Identify the preparation type.
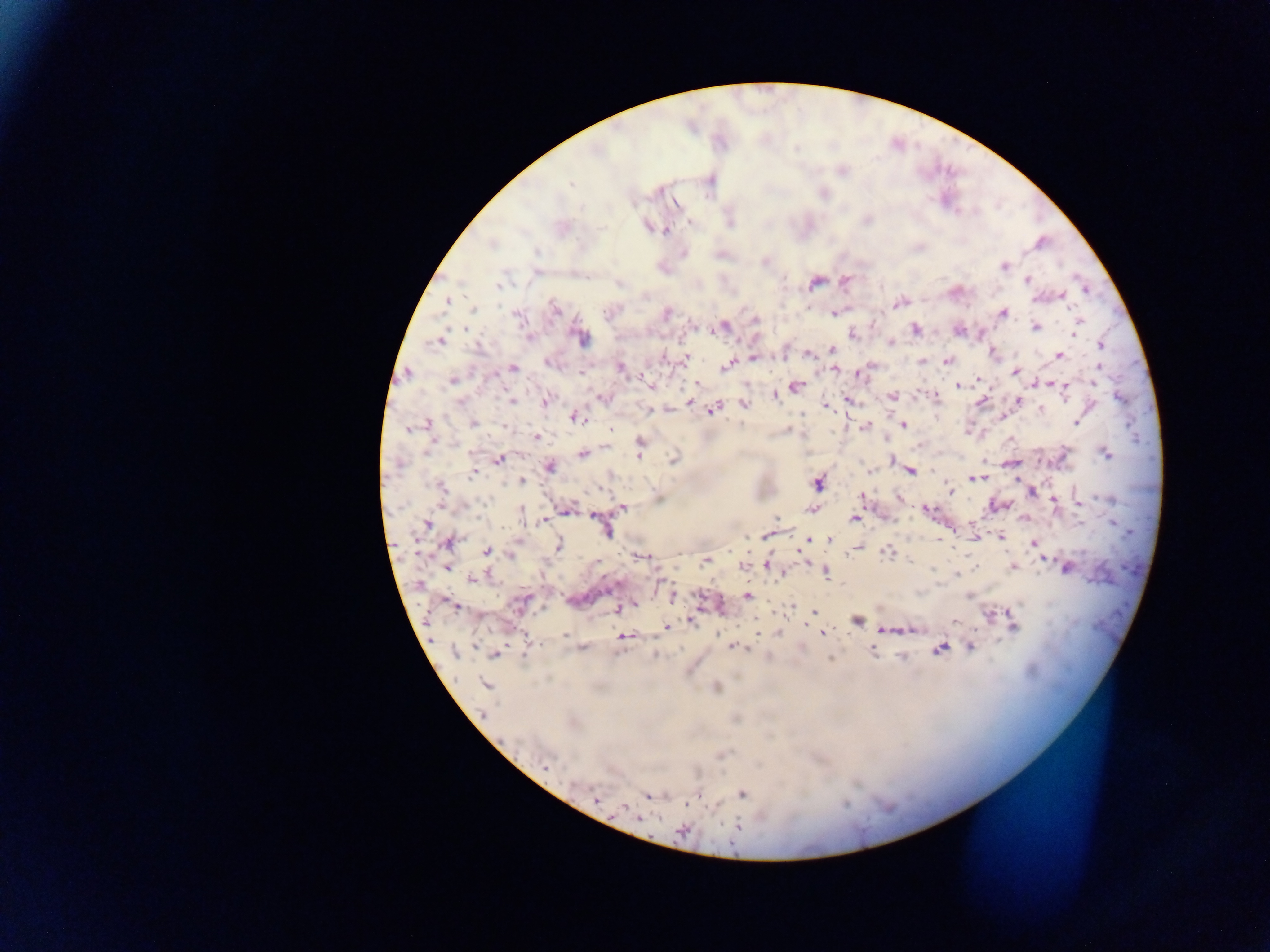
Thick blood film.

{
  "image_size": "1270×952 pixels",
  "field_of_view": "single",
  "country": "Ghana",
  "malaria_parasite_locations": "approximate centers as {x, y} in pixels: {709, 179}, {570, 184}, {821, 193}, {867, 219}, {689, 222}, {647, 227}, {665, 230}, {1041, 243}, {683, 252}, {765, 261}, {1002, 266}, {537, 273}, {844, 280}, {1027, 280}, {814, 282}, {499, 286}, {1061, 295}, {446, 301}, {899, 301}, {555, 309}, {665, 312}, {834, 312}, {1002, 313}, {517, 315}, {755, 319}, {1078, 323}, {722, 327}, {1034, 327}, {958, 329}, {914, 330}, {1075, 331}, {853, 333}, {581, 336}, {529, 338}, {440, 339}, {890, 342}, {1100, 346}, {831, 350}, {811, 351}, {806, 354}, {993, 354}, {1058, 355}, {663, 356}, {753, 357}, {684, 358}, {947, 360}, {922, 361}, {726, 366}, {512, 367}, {620, 367}, {1098, 368}, {835, 369}, {1015, 371}, {583, 372}, {858, 373}, {643, 377}, {453, 379}, {978, 379}, {694, 383}, {1048, 383}, {957, 385}, {1054, 385}, {795, 386}, {652, 387}, {1064, 388}, {774, 394}, {934, 395}, {892, 396}, {604, 397}, {847, 399}, {981, 400}, {1017, 400}, {511, 401}, {545, 401}, {690, 402}, {744, 404}, {826, 406}, {648, 408}, {714, 408}, {1042, 410}, {1002, 415}, {576, 416}, {427, 422}, {1076, 422}, {472, 423}, {903, 424}, {505, 425}, {865, 426}, {408, 428}, {610, 430}, {536, 437}, {639, 440}, {639, 447}, {583, 453}, {1105, 453}, {638, 456}, {498, 459}, {674, 459}, {891, 460}, {1011, 463}, {549, 466}, {909, 470}, {932, 470}, {870, 471}, {472, 473}, {975, 478}, {522, 481}, {817, 481}, {440, 490}, {948, 490}, {861, 496}, {899, 496}, {1053, 499}, {1078, 502}, {997, 504}, {621, 507}, {813, 508}, {566, 509}, {925, 509}, {596, 515}, {776, 517}, {853, 519}, {544, 520}, {426, 523}, {604, 528}, {768, 534}, {999, 536}, {974, 538}, {829, 539}, {806, 540}, {447, 542}, {1034, 543}, {558, 544}, {856, 547}, {487, 550}, {887, 551}, {511, 554}, {639, 555}, {1043, 556}, {706, 560}, {742, 565}, {765, 565}, {446, 566}, {975, 566}, {1012, 566}, {1066, 566}, {825, 569}, {782, 574}, {473, 578}, {419, 584}, {671, 596}, {747, 596}, {524, 600}, {451, 603}, {634, 604}, {792, 607}, {618, 608}, {814, 612}, {987, 613}, {691, 620}, {856, 620}, {956, 622}, {1013, 625}, {666, 628}, {910, 629}, {884, 630}, {758, 632}, {822, 633}, {564, 635}, {625, 636}, {526, 645}, {734, 646}, {969, 646}, {582, 648}, {940, 648}, {871, 649}, {454, 653}, {495, 654}, {655, 654}, {900, 655}, {830, 658}, {485, 683}, {716, 687}, {544, 766}, {698, 793}, {742, 793}, {647, 795}, {595, 800}, {687, 804}, {623, 808}, {639, 818}, {736, 827}, {682, 831}",
  "capture": "mobile-phone photograph through a microscope"
}